Give the extent of all Trypanosoma brucei.
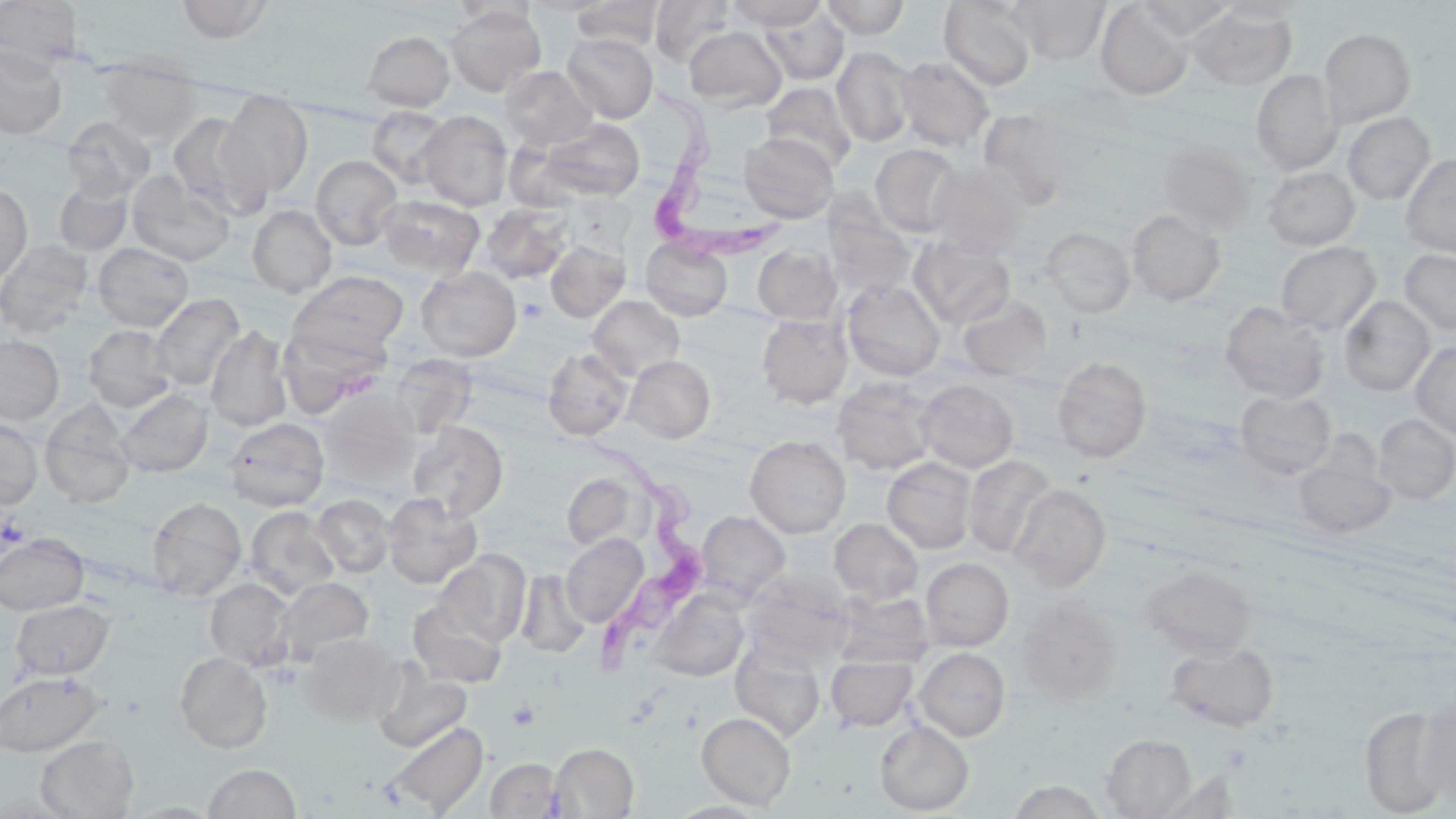
Approximate bounding boxes as (x1, y1, x2, y2) in pixels.
Trypanosoma brucei: (646, 88, 787, 259), (583, 434, 705, 700).

Platelet locations: (518, 298, 548, 323), (1, 514, 27, 549). Uninfected red blood cell locations: (0, 0, 84, 69), (174, 0, 275, 43), (650, 0, 736, 67), (727, 0, 828, 30), (821, 0, 910, 39), (939, 0, 1038, 90), (1010, 0, 1109, 64), (1138, 0, 1235, 40), (1217, 0, 1309, 23), (570, 1, 665, 51), (1096, 2, 1193, 100), (445, 4, 545, 96), (1189, 7, 1297, 89), (761, 8, 849, 86), (684, 26, 786, 111), (1320, 28, 1416, 126), (362, 31, 455, 111), (563, 33, 658, 123), (0, 46, 67, 139), (832, 46, 916, 148), (894, 56, 994, 151), (99, 57, 202, 143), (499, 65, 598, 150), (1251, 69, 1342, 175), (762, 82, 857, 172), (216, 91, 313, 198), (366, 105, 451, 186), (417, 110, 513, 211), (979, 110, 1074, 210), (167, 111, 269, 218), (1343, 112, 1435, 205), (61, 117, 155, 200), (539, 118, 645, 201), (738, 133, 840, 224), (1158, 142, 1256, 233), (871, 143, 965, 236), (1400, 153, 1456, 257), (310, 155, 402, 250), (927, 161, 1029, 257), (1262, 167, 1360, 251), (126, 172, 236, 266), (54, 181, 132, 254), (0, 182, 32, 285), (377, 195, 485, 280), (480, 203, 573, 283), (247, 205, 337, 298), (1127, 209, 1226, 306), (824, 210, 915, 301), (1040, 226, 1136, 319), (909, 235, 1015, 328), (642, 237, 733, 321), (0, 239, 93, 337), (545, 240, 630, 322), (92, 242, 194, 331), (1275, 242, 1381, 334), (753, 245, 842, 324), (1399, 249, 1456, 335), (416, 266, 521, 361), (291, 271, 408, 354), (842, 279, 946, 381), (150, 294, 245, 392), (588, 295, 685, 381), (957, 295, 1053, 379), (1339, 296, 1435, 396), (1219, 302, 1330, 403), (757, 314, 853, 408), (278, 324, 387, 417), (83, 325, 176, 412), (205, 325, 293, 432), (0, 336, 64, 425), (1411, 342, 1456, 439), (543, 347, 634, 441), (624, 355, 716, 443), (1052, 356, 1152, 463), (832, 377, 939, 476), (915, 379, 1019, 473), (115, 389, 213, 477), (1234, 389, 1337, 479), (321, 392, 418, 487), (40, 400, 136, 508), (1373, 414, 1456, 504), (224, 416, 329, 511), (0, 417, 43, 510), (408, 421, 508, 520), (745, 435, 850, 539), (1292, 452, 1396, 540), (963, 454, 1056, 558), (882, 457, 978, 554), (561, 472, 641, 550), (1010, 484, 1111, 590), (382, 492, 481, 589), (312, 494, 395, 577), (147, 497, 247, 601), (244, 506, 339, 597), (695, 510, 790, 603), (830, 517, 923, 605), (0, 533, 89, 615), (560, 533, 648, 628), (435, 550, 531, 646), (921, 557, 1014, 650), (1141, 564, 1256, 660), (516, 570, 590, 658), (276, 577, 373, 664), (205, 578, 295, 670), (651, 590, 749, 681), (833, 592, 934, 669), (10, 599, 114, 680), (407, 599, 507, 688), (1016, 599, 1122, 703), (299, 633, 402, 726), (730, 637, 826, 744), (1167, 641, 1279, 732), (914, 647, 1010, 741), (174, 652, 272, 753), (826, 656, 917, 731), (372, 664, 472, 753), (1, 670, 104, 756), (1418, 694, 1456, 806), (1358, 705, 1451, 817), (697, 711, 796, 810), (383, 720, 489, 816), (874, 720, 974, 815), (1102, 734, 1197, 818), (35, 735, 139, 818), (550, 743, 639, 818), (485, 758, 564, 818), (203, 763, 300, 818), (1159, 770, 1242, 818), (1007, 780, 1106, 818). Slide-level diagnosis: Trypanosoma brucei. Image is 1456×819 pixels. Thin blood film. Single field of view. 1000x magnification. May-Grünwald-Giemsa stain. Light microscopy.